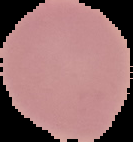
malaria status = uninfected
preparation = thin blood film
image size = 133×142 pixels
image type = cell region segmented out of the field of view; surrounding area masked to black